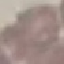

malaria status = uninfected
stain = Giemsa
image type = cell patch, automatically extracted from a larger field of view and resized to 64 × 64 pixels
capture = smartphone camera at the microscope eyepiece
preparation = thin smear